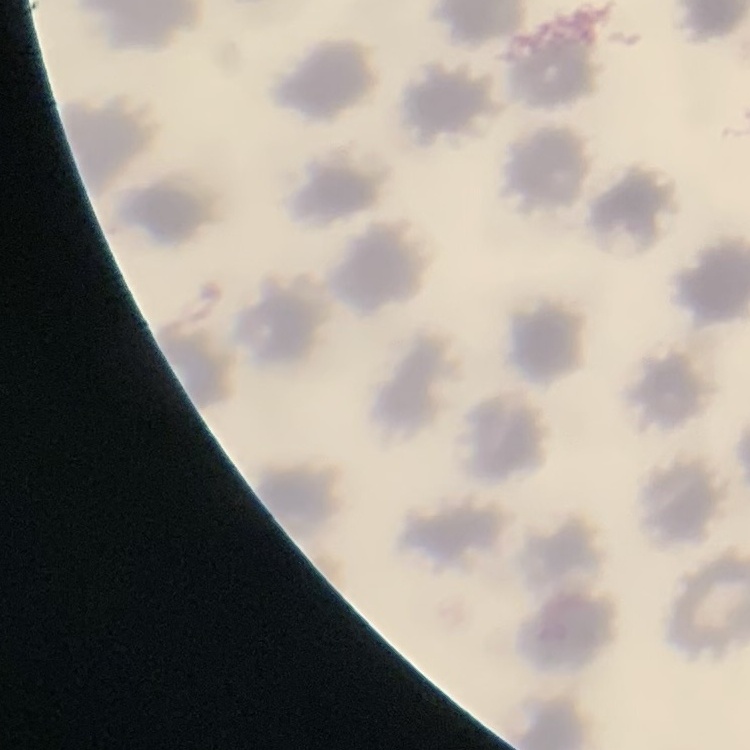

The erythrocytes show no rouleaux formation. Stained with either Field's or Giemsa. One tile cut from a larger photomicrograph. Thin peripheral smear.